Classify this cell by malaria status.
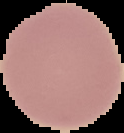
Uninfected.

Image is 124×133 pixels. The area outside the segmented cell region is set to black. From a thin blood smear.